Comment on the morphology of the red blood cells.
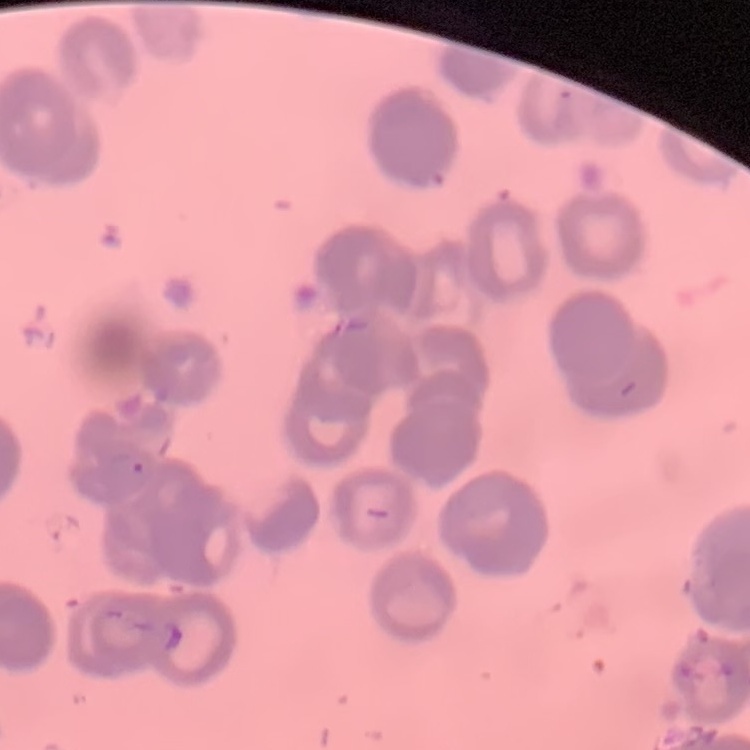

Rouleaux formation.

preparation = thin peripheral smear
image type = square crop of a larger photomicrograph
stain = Field's or Giemsa